Classify this cell by malaria status.
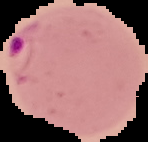

Parasitized.

{
  "image_type": "segmented cell region with the area outside set to black",
  "image_size": "148×142 pixels",
  "preparation": "thin blood film"
}